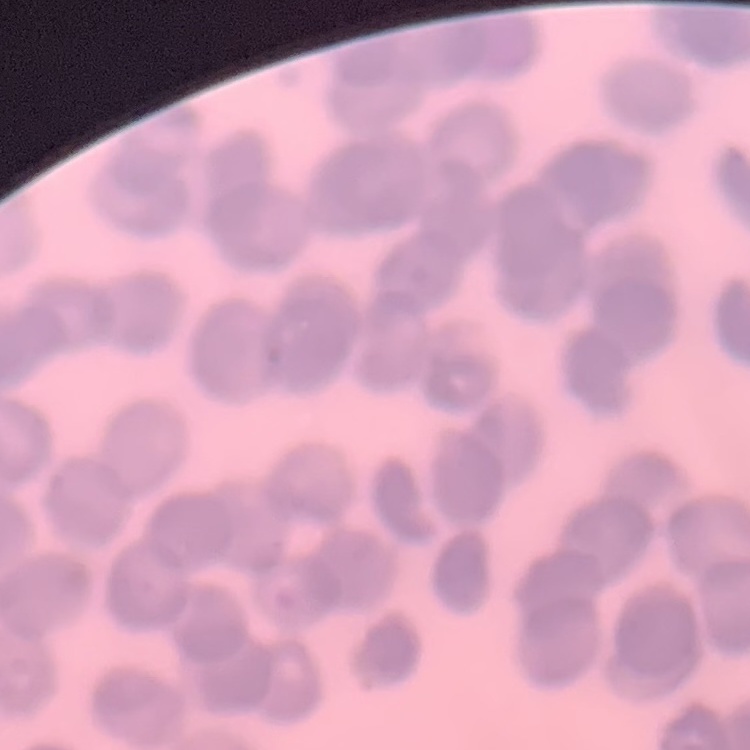

{
  "erythrocyte_morphology": "rouleaux formation",
  "preparation": "thin peripheral smear",
  "image_type": "square crop of a larger photomicrograph",
  "stain": "Field's or Giemsa"
}